Assess this cell for malaria.
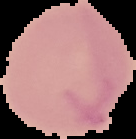

Uninfected.

preparation: thin blood smear
image_type: segmented cell region with the area outside set to black
image_size: 136×139 pixels